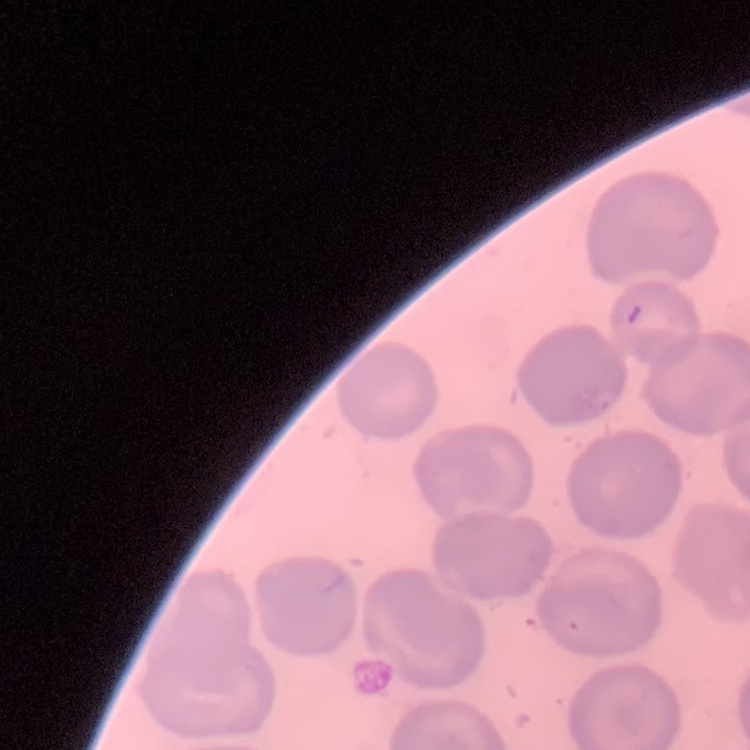

Summary:
  - Erythrocyte morphology: no rouleaux formation
  - Stain: Field's or Giemsa
  - Image type: one tile cut from a larger photomicrograph
  - Preparation: thin peripheral smear